Point out each Plasmodium parasite.
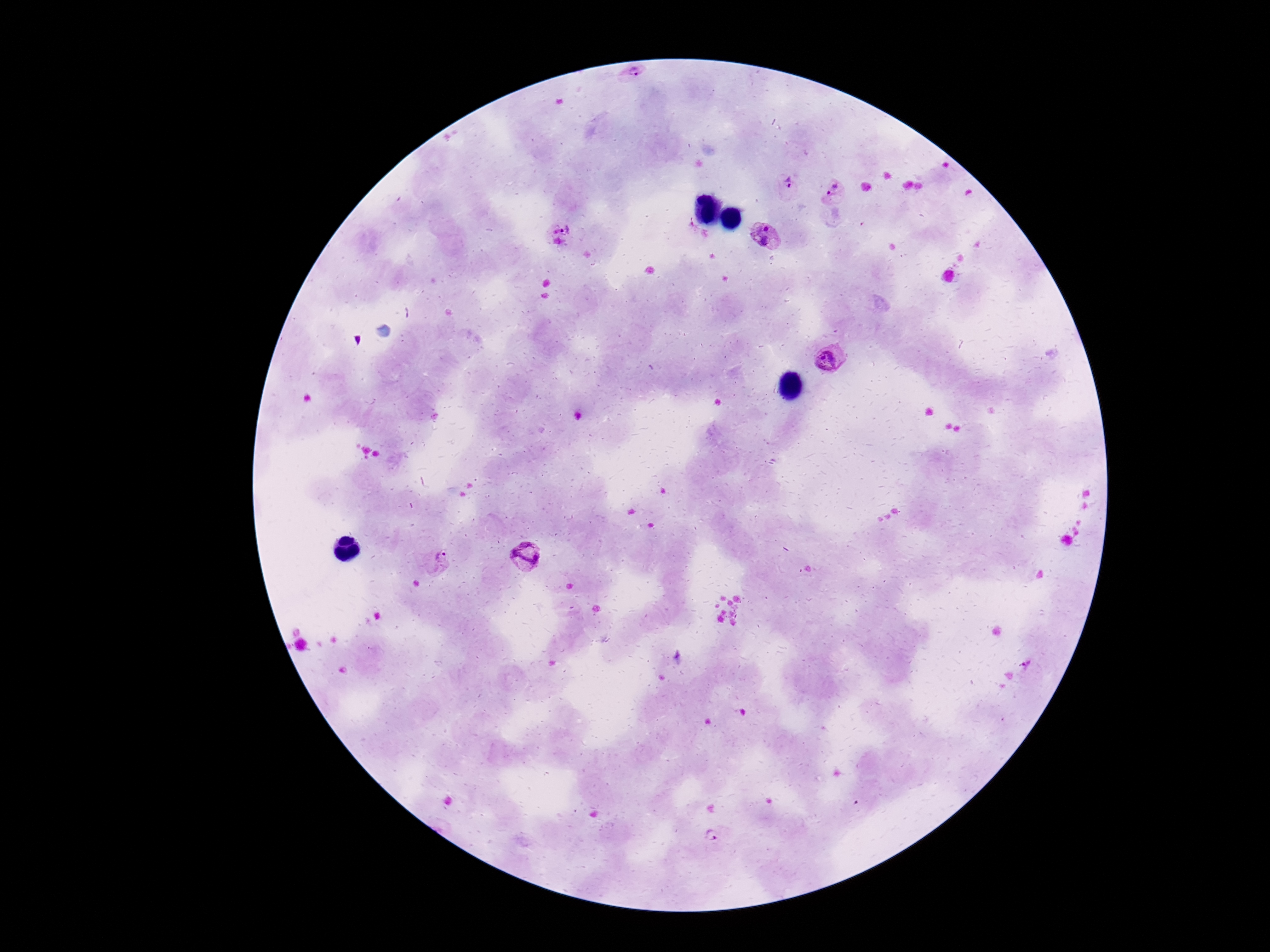

Approximate centers as [x, y] in pixels.
Plasmodium parasites: [636, 75], [789, 186], [834, 192], [561, 235], [768, 235], [830, 358], [526, 557], [432, 562], [713, 836].

image size = 1270×952 pixels
preparation = thick peripheral-blood smear
magnification = 100x
capture = smartphone camera through the microscope eyepiece
stain = Giemsa
patient malaria status = infected
field of view = single